Describe the morphology of the red blood cells.
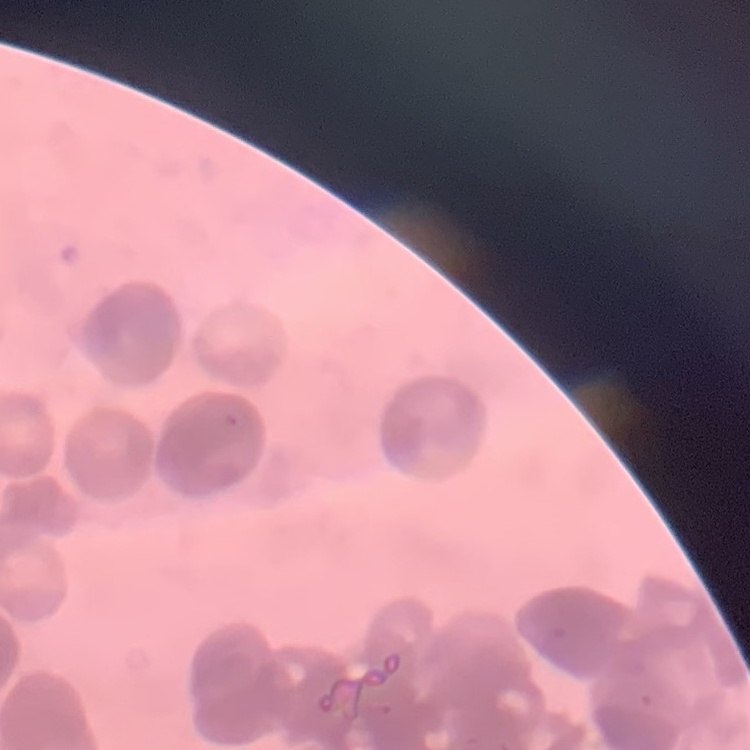

They show rouleaux formation.

Summary:
  - Image type: one tile cut from a larger photomicrograph
  - Preparation: thin blood film
  - Stain: Field's or Giemsa